Comment on the morphology of the red blood cells.
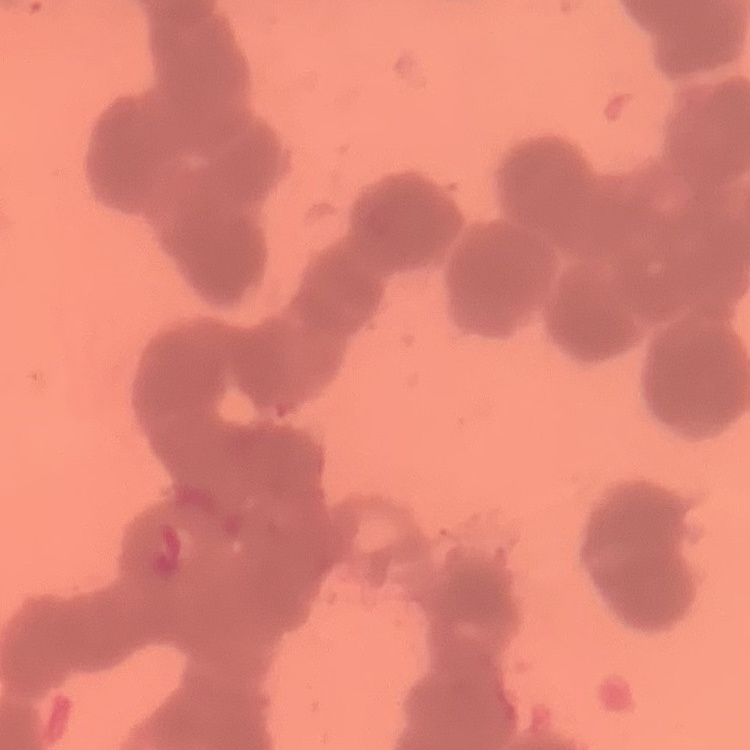
They show rouleaux formation.

preparation = thin peripheral smear
image type = square crop of a larger photomicrograph
stain = Field's or Giemsa